Give the location of every parasitized red blood cell.
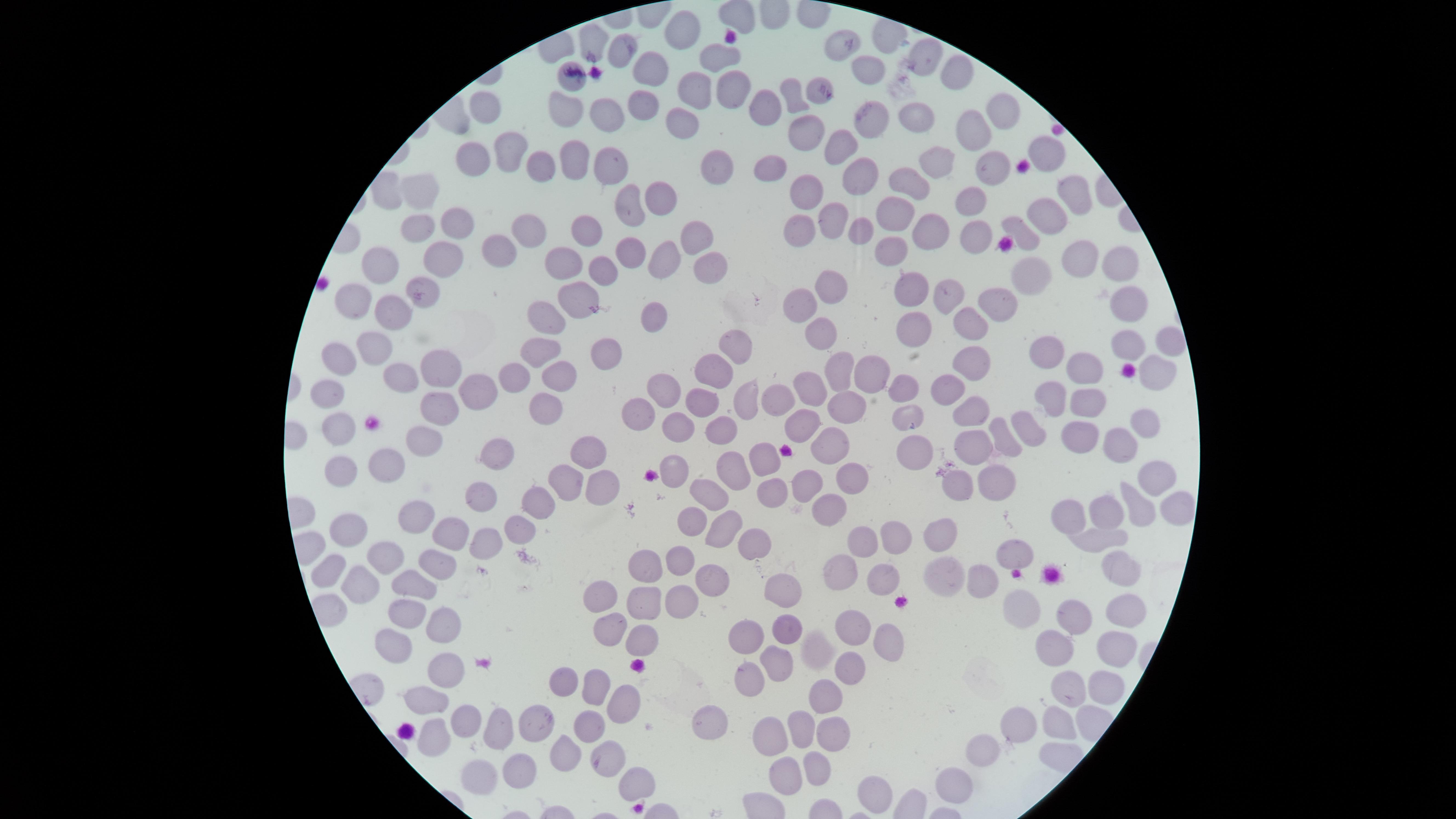

No parasitized red blood cells identified.

visible region = circular
preparation = thin smear of blood
capture = smartphone photograph through the microscope eyepiece
field of view = single
image size = 1456×819 pixels
stain = Giemsa
uninfected red blood cells = approximate marker points as [x, y] in pixels: [678, 27], [592, 40], [841, 48], [617, 53], [927, 54], [719, 56], [645, 68], [960, 72], [868, 75], [690, 86], [728, 88], [815, 91], [643, 101], [789, 105], [561, 106], [482, 109], [757, 109], [1008, 112], [867, 115], [918, 115], [604, 116], [967, 124], [685, 125], [807, 133], [838, 145], [508, 147], [1046, 151], [471, 156], [572, 159], [938, 161], [986, 162], [607, 164], [540, 165], [716, 166], [771, 167], [856, 175], [911, 181], [422, 192], [800, 192], [1075, 195], [972, 199], [655, 200], [626, 208], [893, 211], [1048, 213], [831, 218], [459, 222], [413, 225], [590, 225], [1020, 227], [523, 229], [798, 231], [860, 231], [697, 232], [934, 232], [976, 237], [501, 249], [631, 249], [893, 251], [442, 252], [1076, 256], [664, 259], [565, 262], [389, 263], [600, 263], [706, 267], [1123, 267], [1035, 273], [909, 288], [833, 289], [572, 292], [948, 293], [356, 294], [422, 294], [993, 300], [1126, 301], [802, 306], [394, 307], [970, 317], [650, 319], [920, 321], [548, 325], [822, 336], [1127, 342], [1169, 342], [372, 346], [541, 348], [1048, 348], [613, 352], [738, 352], [344, 355], [968, 356], [1084, 366], [445, 369], [836, 369], [865, 371], [1155, 371], [400, 373], [718, 373], [516, 375], [559, 375], [485, 388], [905, 388], [664, 389], [811, 389], [946, 389], [331, 391], [1050, 395], [782, 398], [744, 399], [1088, 399], [700, 400], [436, 405], [547, 408], [850, 408], [642, 410], [906, 412], [974, 412], [1141, 417], [802, 420], [338, 422], [678, 425], [720, 426], [1023, 426], [1079, 432], [1000, 437], [1116, 440], [831, 443], [424, 446], [974, 447], [586, 448], [911, 449], [765, 455], [498, 456], [389, 468], [676, 471], [344, 475], [729, 475], [1157, 475], [806, 477], [849, 478], [954, 481], [997, 481], [562, 484], [597, 488], [768, 492], [710, 496], [480, 501], [538, 505], [832, 505], [1136, 505], [1107, 510], [1167, 510], [1072, 514], [693, 517], [346, 520], [417, 520], [727, 528], [449, 530], [509, 530], [864, 534], [890, 534], [943, 534], [1101, 539], [483, 546], [746, 546], [1017, 552], [394, 557], [678, 561], [330, 566], [942, 568], [437, 569], [1110, 570], [645, 574], [976, 575], [838, 577], [708, 579], [352, 581], [878, 581], [778, 589], [412, 590], [599, 599], [683, 601], [1023, 606], [642, 610], [1072, 611], [1115, 616], [408, 617], [855, 623], [441, 626], [784, 629], [615, 631], [753, 631], [885, 639], [641, 644], [393, 645], [815, 648], [1047, 649], [1106, 654], [773, 665], [441, 668], [846, 675], [565, 683], [1097, 683], [745, 684], [595, 686], [1056, 693], [824, 698], [426, 700], [627, 703], [467, 716], [531, 720], [708, 720], [1054, 720], [1013, 722], [435, 727], [801, 727], [499, 728], [590, 732], [832, 734], [771, 742], [987, 749], [562, 754], [608, 755], [812, 765], [526, 766], [486, 771], [782, 771], [952, 781], [635, 786], [870, 788]